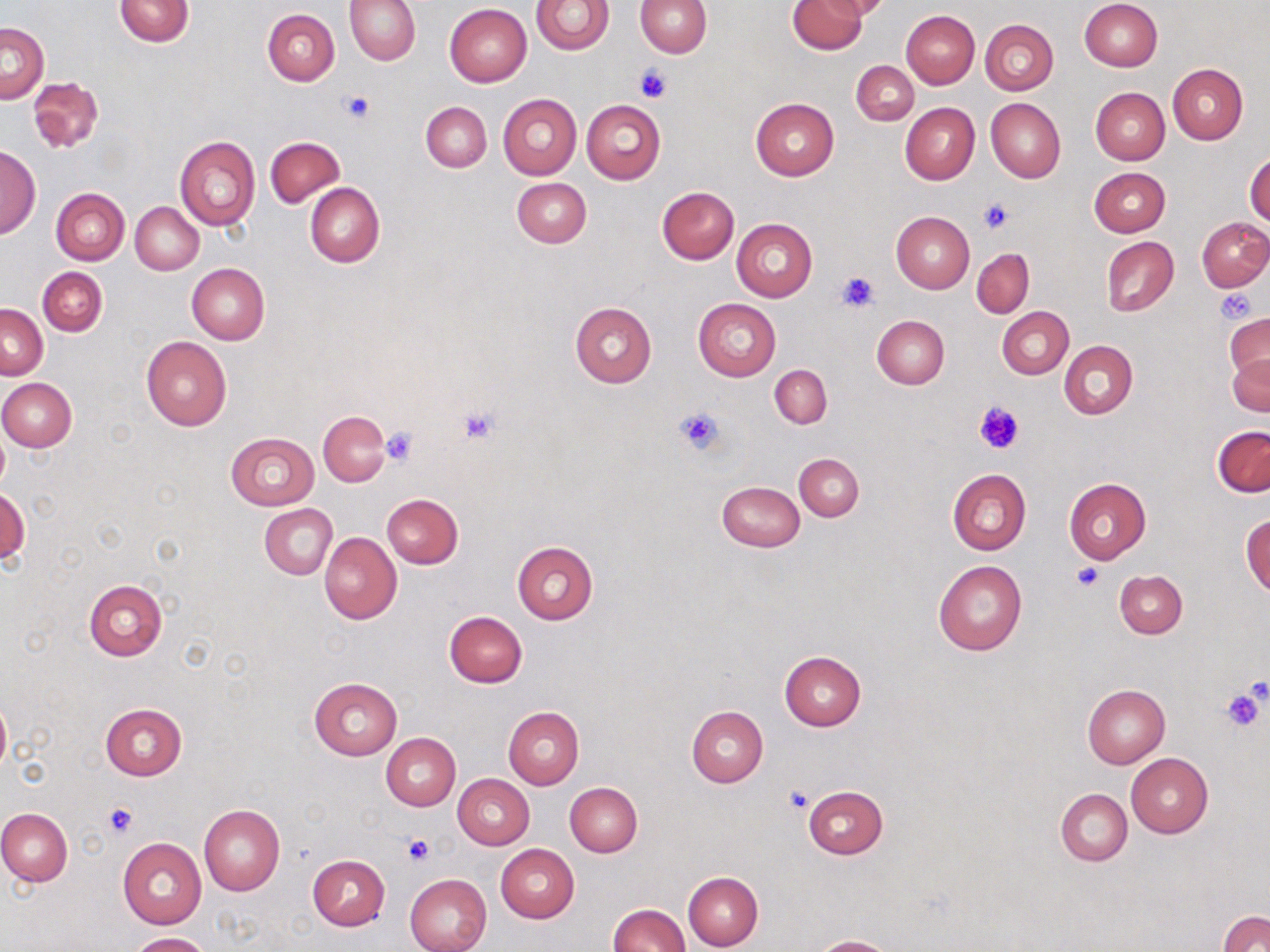

Summary:
  - Coordinate format: approximate bounding boxes as named x1/y1/x2/y2 corners in pixels
  - Platelet locations: (x1=633, y1=65, x2=672, y2=102), (x1=340, y1=91, x2=374, y2=123), (x1=978, y1=198, x2=1014, y2=233), (x1=835, y1=269, x2=878, y2=312), (x1=1216, y1=288, x2=1258, y2=323), (x1=975, y1=399, x2=1025, y2=455), (x1=457, y1=406, x2=502, y2=443), (x1=675, y1=407, x2=725, y2=456), (x1=381, y1=427, x2=418, y2=466), (x1=1073, y1=563, x2=1103, y2=592), (x1=1220, y1=686, x2=1267, y2=734), (x1=783, y1=786, x2=813, y2=814), (x1=104, y1=802, x2=138, y2=837), (x1=402, y1=834, x2=434, y2=867)
  - Uninfected red blood cell locations: (x1=114, y1=0, x2=193, y2=47), (x1=346, y1=0, x2=421, y2=65), (x1=530, y1=0, x2=614, y2=55), (x1=636, y1=0, x2=712, y2=57), (x1=789, y1=0, x2=866, y2=54), (x1=818, y1=0, x2=891, y2=21), (x1=1079, y1=0, x2=1162, y2=72), (x1=445, y1=4, x2=532, y2=86), (x1=263, y1=7, x2=340, y2=85), (x1=901, y1=10, x2=980, y2=89), (x1=981, y1=19, x2=1059, y2=94), (x1=1, y1=22, x2=49, y2=103), (x1=851, y1=59, x2=918, y2=124), (x1=1168, y1=64, x2=1248, y2=144), (x1=29, y1=77, x2=103, y2=152), (x1=1091, y1=87, x2=1170, y2=164), (x1=497, y1=94, x2=582, y2=180), (x1=751, y1=98, x2=839, y2=180), (x1=986, y1=98, x2=1065, y2=183), (x1=581, y1=99, x2=666, y2=183), (x1=420, y1=101, x2=491, y2=172), (x1=901, y1=103, x2=980, y2=184), (x1=265, y1=136, x2=344, y2=207), (x1=175, y1=137, x2=260, y2=230), (x1=0, y1=147, x2=41, y2=237), (x1=1246, y1=151, x2=1270, y2=228), (x1=1090, y1=167, x2=1171, y2=237), (x1=512, y1=177, x2=591, y2=247), (x1=305, y1=183, x2=384, y2=268), (x1=656, y1=187, x2=739, y2=264), (x1=51, y1=188, x2=129, y2=265), (x1=130, y1=202, x2=204, y2=275), (x1=891, y1=212, x2=974, y2=292), (x1=1198, y1=217, x2=1270, y2=291), (x1=732, y1=218, x2=816, y2=301), (x1=1101, y1=236, x2=1178, y2=317), (x1=973, y1=248, x2=1035, y2=317), (x1=187, y1=264, x2=269, y2=345), (x1=38, y1=266, x2=107, y2=336), (x1=692, y1=298, x2=781, y2=381), (x1=570, y1=302, x2=657, y2=388), (x1=1, y1=304, x2=48, y2=380), (x1=998, y1=307, x2=1074, y2=379), (x1=1226, y1=310, x2=1270, y2=393), (x1=872, y1=316, x2=949, y2=389), (x1=141, y1=337, x2=232, y2=432), (x1=1060, y1=340, x2=1138, y2=419), (x1=1228, y1=350, x2=1270, y2=417), (x1=769, y1=364, x2=831, y2=429), (x1=0, y1=378, x2=76, y2=451), (x1=319, y1=411, x2=390, y2=485), (x1=0, y1=424, x2=9, y2=496), (x1=1213, y1=427, x2=1270, y2=498), (x1=226, y1=432, x2=319, y2=510), (x1=794, y1=454, x2=863, y2=521), (x1=947, y1=469, x2=1030, y2=556), (x1=1064, y1=477, x2=1151, y2=563), (x1=717, y1=481, x2=805, y2=552), (x1=1, y1=488, x2=30, y2=567), (x1=381, y1=493, x2=463, y2=568), (x1=259, y1=504, x2=336, y2=579), (x1=1242, y1=513, x2=1270, y2=596), (x1=319, y1=531, x2=401, y2=624), (x1=511, y1=541, x2=599, y2=625), (x1=934, y1=561, x2=1027, y2=656), (x1=1115, y1=570, x2=1187, y2=639), (x1=83, y1=579, x2=166, y2=661), (x1=444, y1=610, x2=527, y2=687), (x1=779, y1=652, x2=866, y2=730), (x1=308, y1=677, x2=402, y2=760), (x1=1082, y1=684, x2=1171, y2=769), (x1=0, y1=695, x2=11, y2=777), (x1=100, y1=703, x2=188, y2=780), (x1=503, y1=706, x2=584, y2=789), (x1=686, y1=706, x2=768, y2=788), (x1=381, y1=733, x2=461, y2=810), (x1=1126, y1=753, x2=1213, y2=837), (x1=454, y1=775, x2=534, y2=849), (x1=565, y1=783, x2=642, y2=856), (x1=803, y1=785, x2=887, y2=859), (x1=1055, y1=789, x2=1132, y2=866), (x1=199, y1=806, x2=285, y2=895), (x1=0, y1=808, x2=73, y2=886), (x1=118, y1=838, x2=207, y2=928), (x1=495, y1=844, x2=579, y2=923), (x1=307, y1=854, x2=389, y2=931), (x1=683, y1=871, x2=764, y2=950), (x1=405, y1=874, x2=491, y2=952), (x1=608, y1=904, x2=689, y2=952), (x1=1219, y1=911, x2=1270, y2=952), (x1=126, y1=932, x2=210, y2=951), (x1=813, y1=935, x2=895, y2=952)
  - Slide-level diagnosis: negative for blood parasites
  - Stain: May-Grünwald-Giemsa
  - Magnification: 1000x
  - Image size: 1270×952 pixels
  - Field of view: one of a larger specimen
  - Modality: light microscopy
  - Preparation: thin blood smear